Point out each Plasmodium parasite.
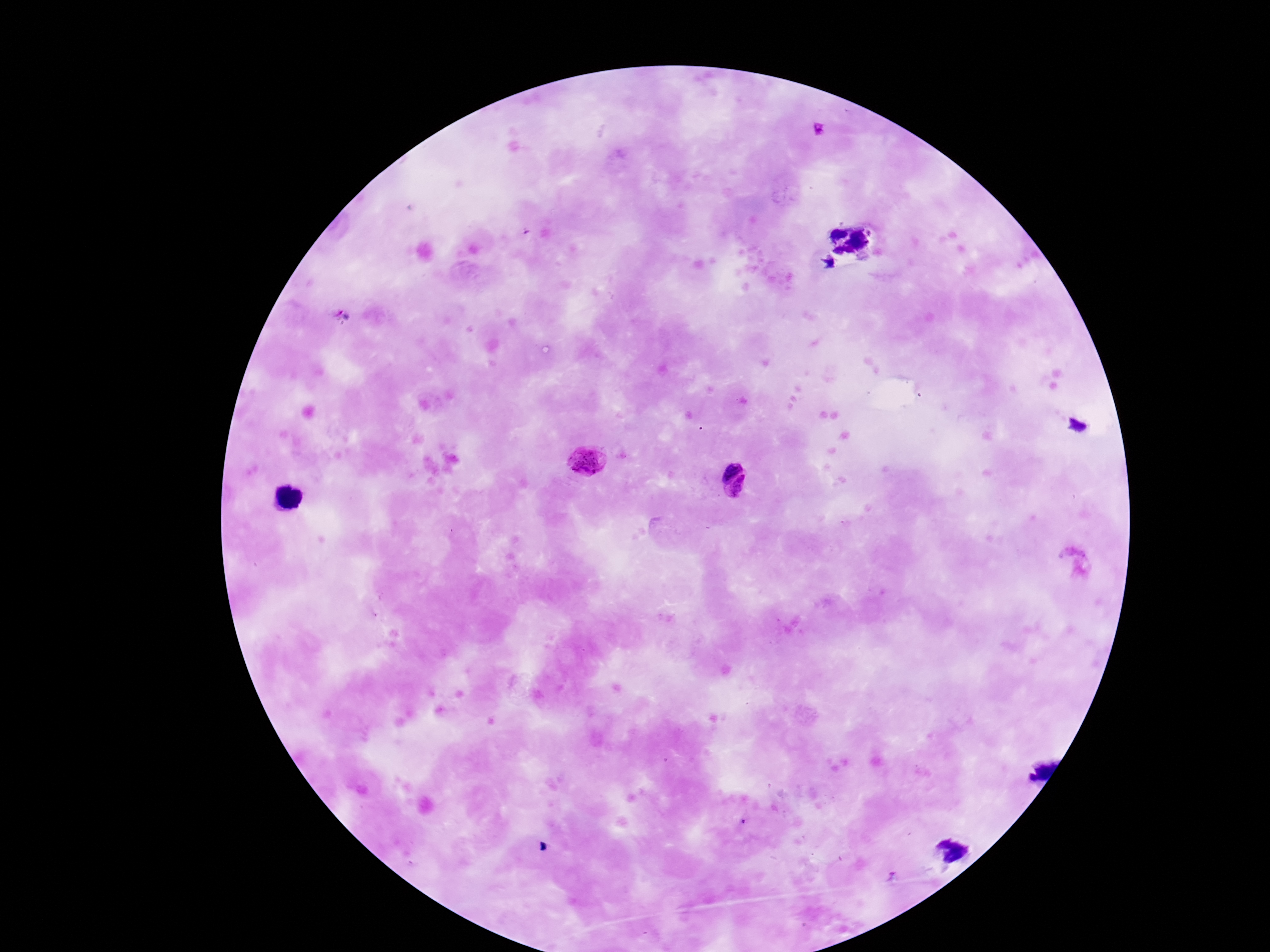
Approximate centers as (x, y) in pixels.
Plasmodium parasites: (821, 128), (587, 463), (725, 463), (745, 498).

Summary:
  - Preparation: thick peripheral-blood smear
  - Patient malaria status: positive
  - Image size: 1270×952 pixels
  - Stain: Giemsa
  - Capture: smartphone camera through the microscope eyepiece
  - Magnification: 100x
  - Field of view: one from this slide